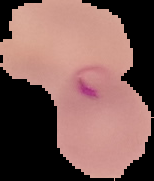
Cell region segmented out of the field of view; the surrounding area is masked to black. Malaria status: parasitized. From a thin blood film. Image is 154×181 pixels.